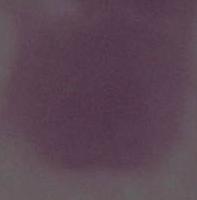
Summary:
  - Identification: red blood cell
  - Modality: micrograph
  - Magnification: 1000x